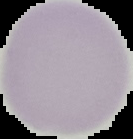

preparation = thin blood smear
image type = cell region segmented out of the field of view; surrounding area masked to black
image size = 133×139 pixels
malaria status = uninfected